Classify this cell by malaria status.
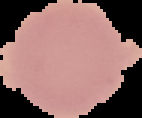
It is uninfected.

Image is 142×118 pixels. The area outside the segmented cell region is set to black. From a thin blood smear.